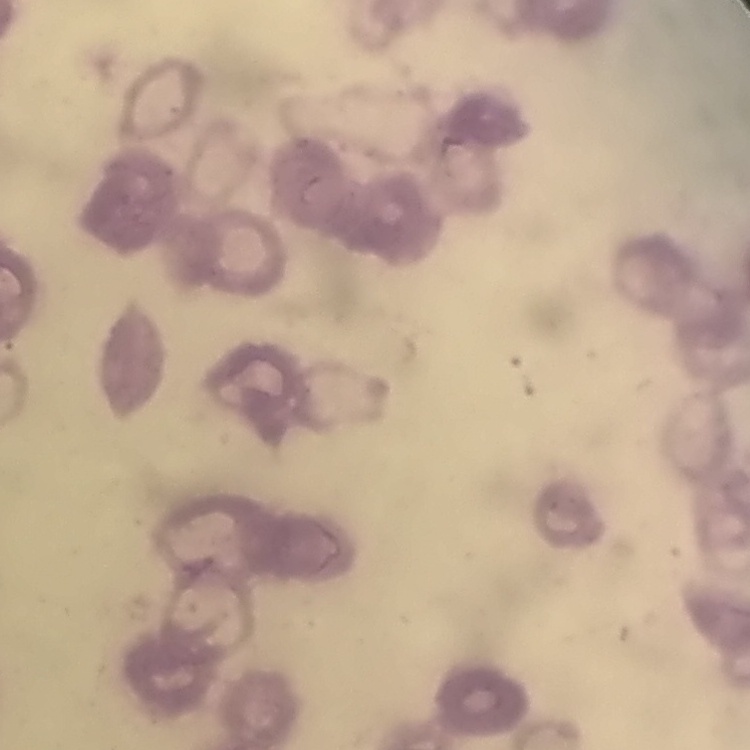

The erythrocytes show rouleaux formation. Thin peripheral smear. Square crop of a larger photomicrograph. Field's or Giemsa stain.